Point out every malaria parasite.
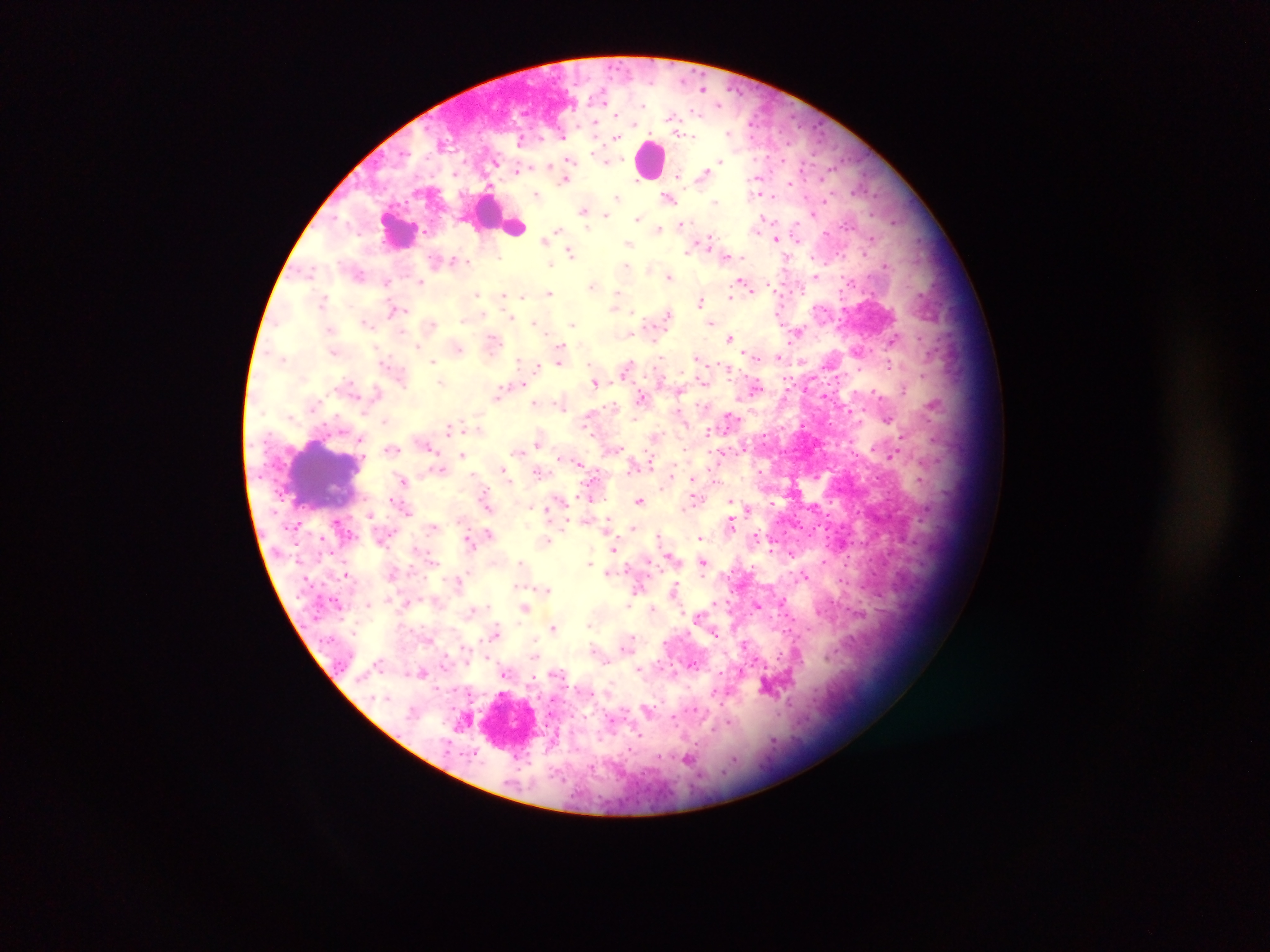

Approximate centers as x y in pixels.
Malaria parasites: 701 87; 698 113; 667 117; 596 123; 748 123; 818 129; 730 132; 753 137; 616 138; 788 145; 572 161; 720 161; 551 163; 518 171; 703 171; 758 179; 821 179; 566 180; 634 182; 790 184; 853 190; 538 193; 760 194; 616 196; 670 198; 717 201; 823 202; 583 211; 607 215; 813 215; 638 219; 765 219; 896 220; 513 224; 560 227; 660 227; 587 228; 823 233; 708 238; 775 239; 543 240; 798 240; 630 243; 687 250; 570 251; 836 253; 864 253; 844 255; 455 261; 550 264; 824 264; 884 265; 627 267; 648 268; 669 276; 841 276; 814 277; 421 281; 741 281; 746 283; 387 284; 593 284; 753 289; 801 290; 839 290; 861 291; 550 292; 616 293; 872 293; 479 294; 521 295; 503 296; 730 298; 322 300; 701 300; 614 305; 780 306; 398 311; 632 312; 670 313; 391 314; 512 317; 534 321; 711 321; 464 322; 367 323; 573 323; 782 324; 629 333; 799 333; 730 337; 892 342; 561 343; 417 346; 460 347; 862 351; 562 354; 658 354; 746 356; 778 357; 695 359; 890 360; 434 361; 558 362; 718 362; 520 363; 803 363; 893 363; 536 367; 859 370; 920 375; 835 376; 728 380; 441 382; 595 384; 378 388; 757 389; 498 393; 641 394; 876 395; 824 396; 535 403; 934 405; 850 410; 730 420; 385 421; 829 423; 803 425; 450 427; 583 427; 705 431; 764 434; 901 439; 932 439; 360 440; 538 444; 682 448; 646 449; 433 450; 519 453; 853 454; 462 455; 720 455; 893 455; 579 463; 652 465; 504 469; 537 471; 759 471; 402 478; 693 479; 640 499; 478 500; 564 500; 733 501; 828 502; 770 503; 689 504; 546 510; 926 510; 368 514; 826 514; 337 520; 606 521; 461 522; 567 523; 731 524; 433 525; 632 527; 815 527; 824 529; 488 532; 701 536; 660 537; 548 540; 471 547; 614 549; 770 549; 671 553; 790 556; 646 559; 824 559; 704 562; 521 563; 591 564; 846 566; 627 567; 609 572; 343 574; 806 575; 458 578; 839 581; 306 582; 546 589; 638 589; 674 590; 779 599; 713 602; 367 603; 628 604; 487 605; 757 606; 526 607; 653 609; 793 619; 590 624; 553 628; 786 630; 494 634; 716 635; 631 638; 480 641; 461 647; 627 647; 593 648; 536 656; 777 659; 639 669; 548 671; 425 672; 507 673; 532 678; 565 680; 766 686; 468 692; 714 692; 720 705; 696 710; 673 716; 610 720; 728 723; 640 735; 772 739; 628 747; 474 752; 514 756; 658 757; 734 759; 689 760.

Thick blood film. Sample from Ghana. Photographed through a microscope with a mobile-phone camera. Image is 1270×952 pixels. Single field of view.